State which parasite is depicted.
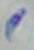
This is Toxoplasma gondii.

modality = photomicrograph
magnification = 1000x